State which parasite is depicted.
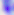
Toxoplasma gondii.

400x magnification. Photomicrograph.